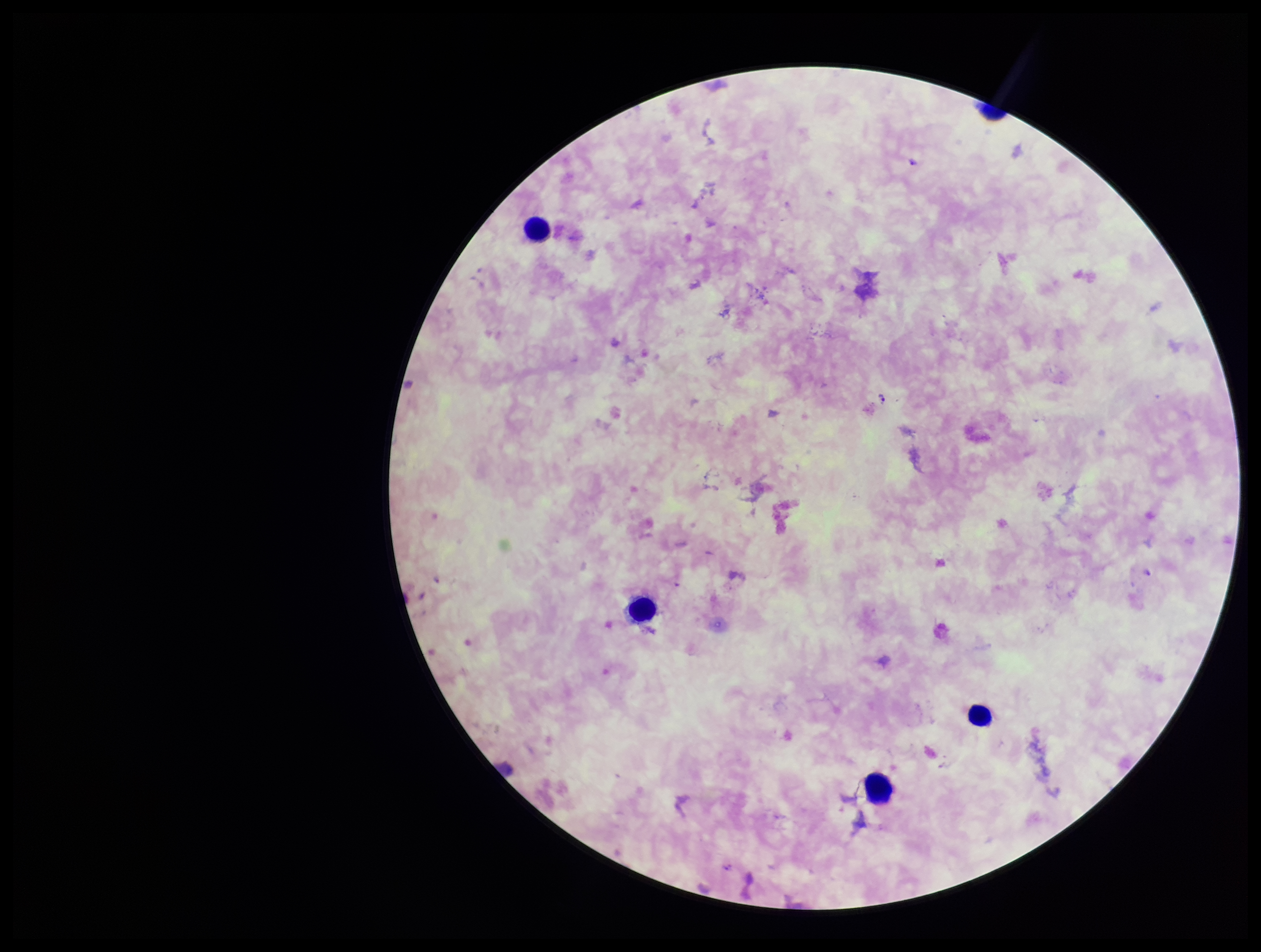
parasite_count: 1
leukocyte_count: 4
species_reported_for_this_patient: Plasmodium falciparum
plasmodium_parasites: detected
preparation: thick smear
field_of_view: one from this slide
image_size: 1261×952 pixels
patient_malaria_status: infected
capture: smartphone photograph through the microscope eyepiece
stain: Giemsa